Assess this cell for malaria.
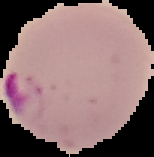
It is parasitized.

Image is 154×157 pixels. Cell region segmented out of the field of view; the surrounding area is masked to black. From a thin blood film.